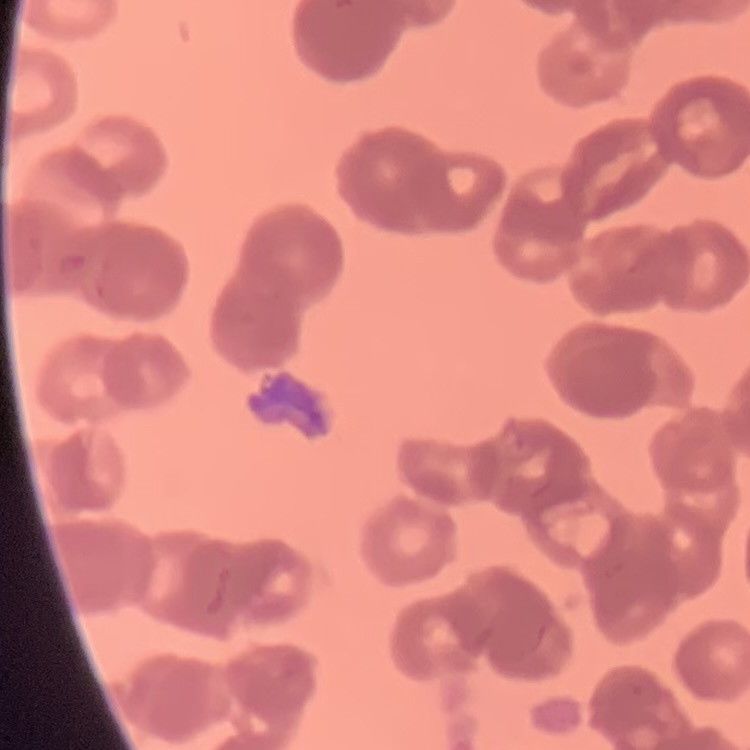
Summary:
  - Erythrocyte morphology: rouleaux formation
  - Stain: Field's or Giemsa
  - Image type: square crop of a larger photomicrograph
  - Preparation: thin blood film